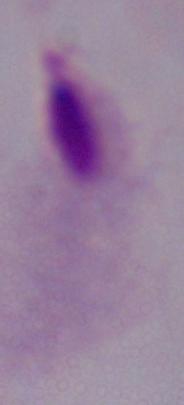
magnification = 1000x
identification = trichomonad
modality = photomicrograph